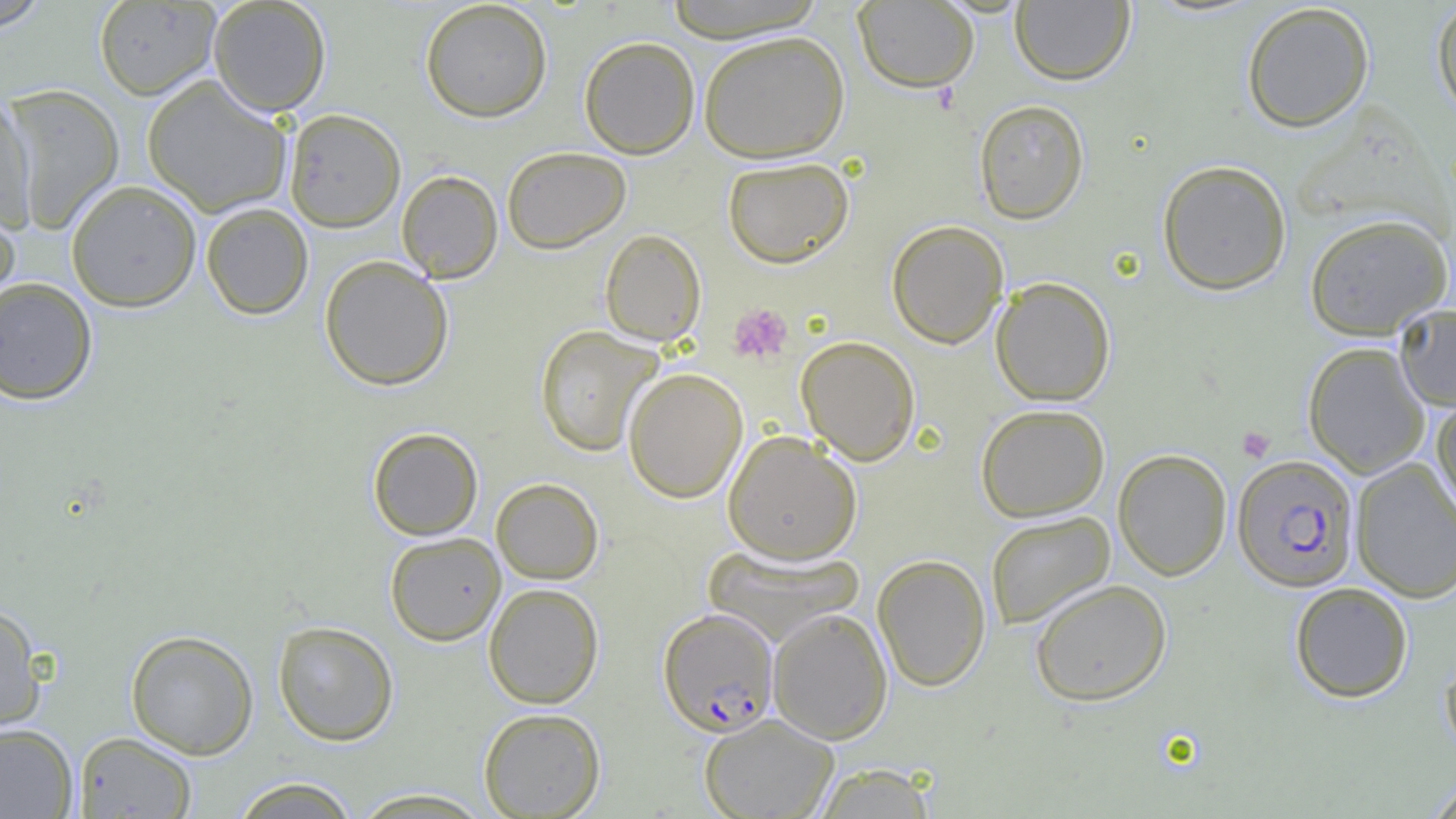
Approximate bounding boxes as (x1, y1, x2, y2) in pixels. Platelet locations: (727, 302, 793, 365), (1238, 426, 1275, 462). Plasmodium falciparum-infected red blood cell locations: (1232, 455, 1359, 592), (658, 608, 779, 737). Uninfected red blood cell locations: (0, 0, 55, 34), (208, 0, 331, 116), (419, 0, 553, 122), (663, 0, 828, 42), (853, 0, 979, 92), (1010, 0, 1135, 85), (93, 1, 222, 100), (1431, 1, 1456, 122), (1241, 2, 1375, 132), (698, 30, 850, 162), (579, 36, 700, 159), (142, 75, 292, 217), (3, 82, 125, 235), (0, 91, 37, 230), (973, 98, 1089, 224), (284, 108, 406, 232), (502, 146, 631, 253), (722, 157, 853, 268), (1157, 159, 1292, 295), (397, 170, 503, 283), (65, 180, 202, 312), (0, 198, 21, 318), (201, 202, 314, 320), (1303, 213, 1454, 340), (886, 220, 1008, 349), (600, 229, 706, 346), (319, 255, 454, 390), (990, 276, 1116, 406), (0, 277, 98, 405), (1395, 305, 1456, 411), (534, 325, 663, 456), (796, 335, 920, 465), (1303, 341, 1430, 478), (623, 367, 748, 503), (1432, 394, 1456, 525), (975, 403, 1110, 522), (368, 427, 483, 540), (723, 431, 862, 564), (1113, 448, 1232, 581), (1351, 458, 1456, 604), (491, 477, 604, 584), (985, 511, 1115, 629), (384, 532, 506, 646), (702, 546, 864, 643), (872, 554, 991, 692), (1030, 579, 1172, 705), (1289, 582, 1414, 703), (484, 583, 604, 709), (0, 601, 46, 733), (768, 608, 893, 744), (272, 620, 399, 745), (125, 629, 260, 760), (1439, 648, 1456, 761), (478, 707, 606, 818), (699, 713, 839, 819), (0, 723, 78, 818), (73, 731, 197, 818), (812, 763, 936, 818), (230, 776, 362, 818), (1424, 776, 1456, 818), (347, 787, 497, 818). Slide-level diagnosis: Plasmodium falciparum. Thin blood film. Captured at 1000x magnification. Image is 1456×819 pixels. Optical microscopy. Single field of view.